Outline each blood parasite and name the species.
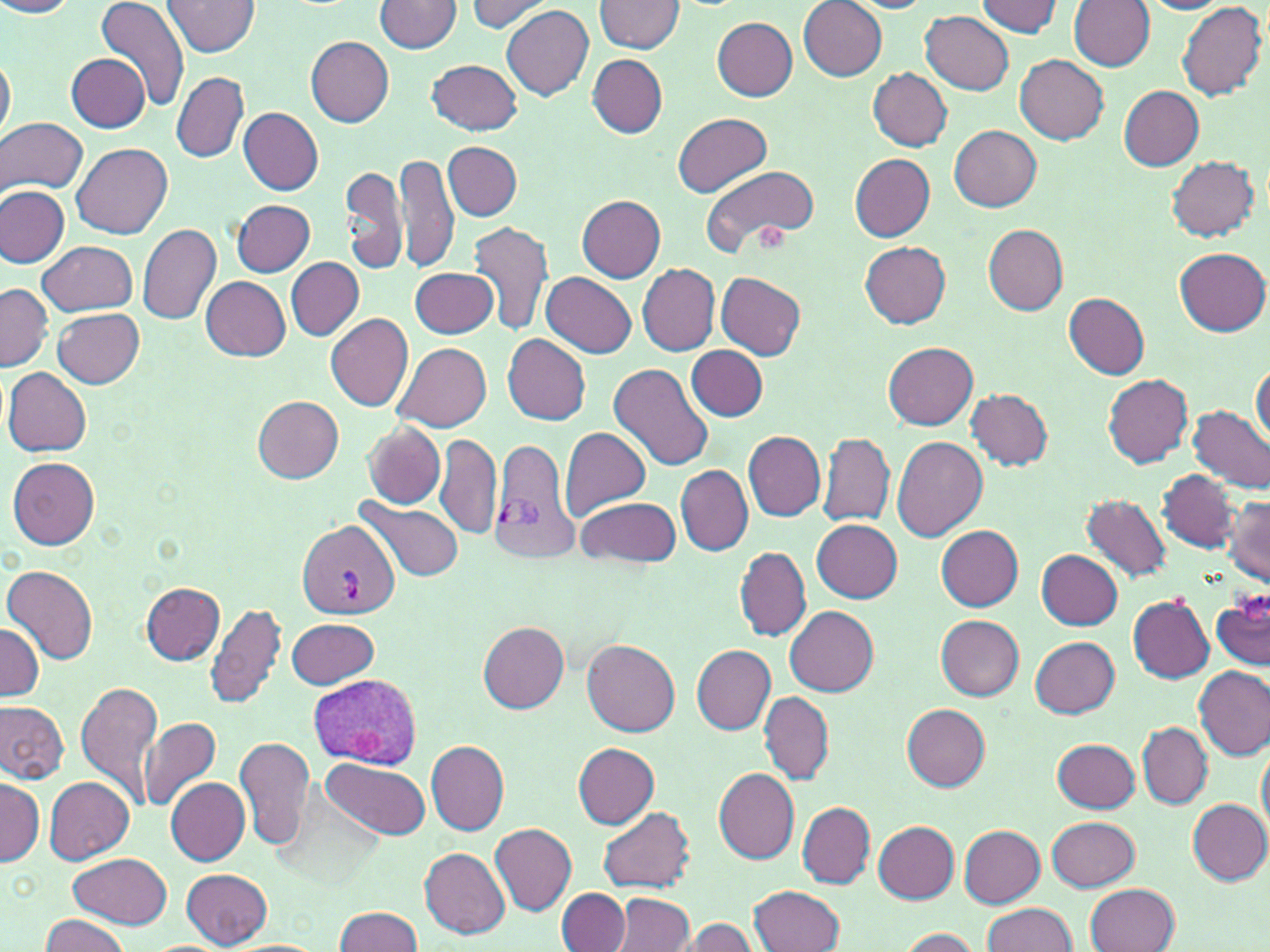
Approximate bounding boxes as (x1,y1)-(x2,y2) corner pairs in pixels.
Plasmodium vivax-infected red blood cells: (490,436)-(578,562), (297,520)-(400,619), (309,673)-(422,768).
No Plasmodium falciparum, Plasmodium ovale, Plasmodium malariae, Babesia divergens, or Trypanosoma brucei observed.

Summary:
  - Uninfected red blood cell locations: (0,0)-(78,19), (165,0)-(259,56), (799,0)-(887,80), (1056,0)-(1151,128), (96,1)-(188,112), (375,1)-(461,53), (463,1)-(554,34), (595,1)-(683,53), (978,1)-(1063,39), (1069,1)-(1155,72), (1137,2)-(1230,15), (1177,2)-(1267,101), (502,4)-(593,102), (920,10)-(1014,94), (712,17)-(798,100), (306,37)-(395,127), (66,52)-(148,131), (1,53)-(15,147), (1014,53)-(1109,143), (588,56)-(668,137), (428,60)-(524,135), (867,67)-(952,151), (172,72)-(248,161), (1119,85)-(1205,169), (239,108)-(324,196), (673,113)-(772,197), (1,117)-(88,196), (949,125)-(1040,211), (443,141)-(522,221), (72,143)-(172,238), (394,151)-(460,275), (850,154)-(936,241), (1167,154)-(1261,241), (341,164)-(408,274), (701,164)-(820,255), (0,186)-(69,268), (577,196)-(665,281), (234,200)-(314,277), (469,220)-(553,336), (982,223)-(1067,316), (137,224)-(221,325), (39,240)-(138,315), (860,242)-(952,328), (1174,247)-(1269,336), (286,257)-(364,340), (637,263)-(720,355), (410,266)-(499,339), (541,272)-(637,358), (715,272)-(807,359), (201,277)-(291,361), (1,284)-(51,370), (1064,293)-(1150,380), (53,307)-(145,387), (325,312)-(415,410), (501,333)-(591,425), (393,341)-(491,431), (884,342)-(977,430), (686,345)-(768,422), (1251,363)-(1269,445), (609,364)-(715,471), (4,368)-(91,457), (1102,373)-(1194,467), (966,387)-(1053,470), (252,396)-(344,483), (1189,406)-(1270,494), (361,422)-(445,509), (559,427)-(652,518), (742,430)-(825,521), (818,432)-(895,527), (436,434)-(502,540), (892,437)-(989,540), (7,457)-(99,549), (675,465)-(751,557), (1159,471)-(1238,552), (580,480)-(753,564), (1081,495)-(1171,583), (577,496)-(680,569), (1224,496)-(1270,585), (357,498)-(465,583), (812,518)-(903,604), (937,526)-(1023,610), (735,547)-(810,640), (1037,550)-(1124,629), (5,564)-(98,662), (142,582)-(225,664), (1212,589)-(1270,671), (1128,596)-(1214,683), (206,602)-(287,710), (786,606)-(879,695), (935,615)-(1024,701), (287,617)-(379,689), (0,620)-(42,702), (478,622)-(569,713), (1032,636)-(1120,718), (582,639)-(680,737), (692,645)-(776,735), (1194,665)-(1269,760), (76,679)-(161,804), (758,691)-(834,786), (0,698)-(70,785), (743,699)-(825,842), (902,703)-(991,790), (139,716)-(220,811), (1138,723)-(1211,808), (235,736)-(313,850), (1053,738)-(1139,813), (1256,738)-(1269,841), (426,740)-(510,835), (572,742)-(661,828), (322,757)-(431,840), (713,767)-(799,865), (0,777)-(43,865), (166,777)-(250,864), (45,778)-(135,865), (1188,800)-(1269,884), (797,802)-(875,889), (596,805)-(697,894), (1046,817)-(1139,891), (874,821)-(960,904), (490,822)-(576,915), (960,825)-(1044,907), (421,848)-(510,938), (69,854)-(172,928), (181,868)-(272,948), (1087,882)-(1180,952), (750,885)-(846,952), (557,889)-(630,951), (613,893)-(694,952), (981,902)-(1078,952), (333,907)-(423,951), (38,915)-(131,952), (678,917)-(758,952), (896,928)-(981,951)
  - Platelet locations: (752,221)-(791,250), (1240,595)-(1270,623)
  - Slide-level diagnosis: Plasmodium vivax
  - Modality: light microscopy
  - Image size: 1270×952 pixels
  - Field of view: single
  - Preparation: thin blood film
  - Stain: May-Grünwald-Giemsa
  - Magnification: 1000x